Name the blood parasite species.
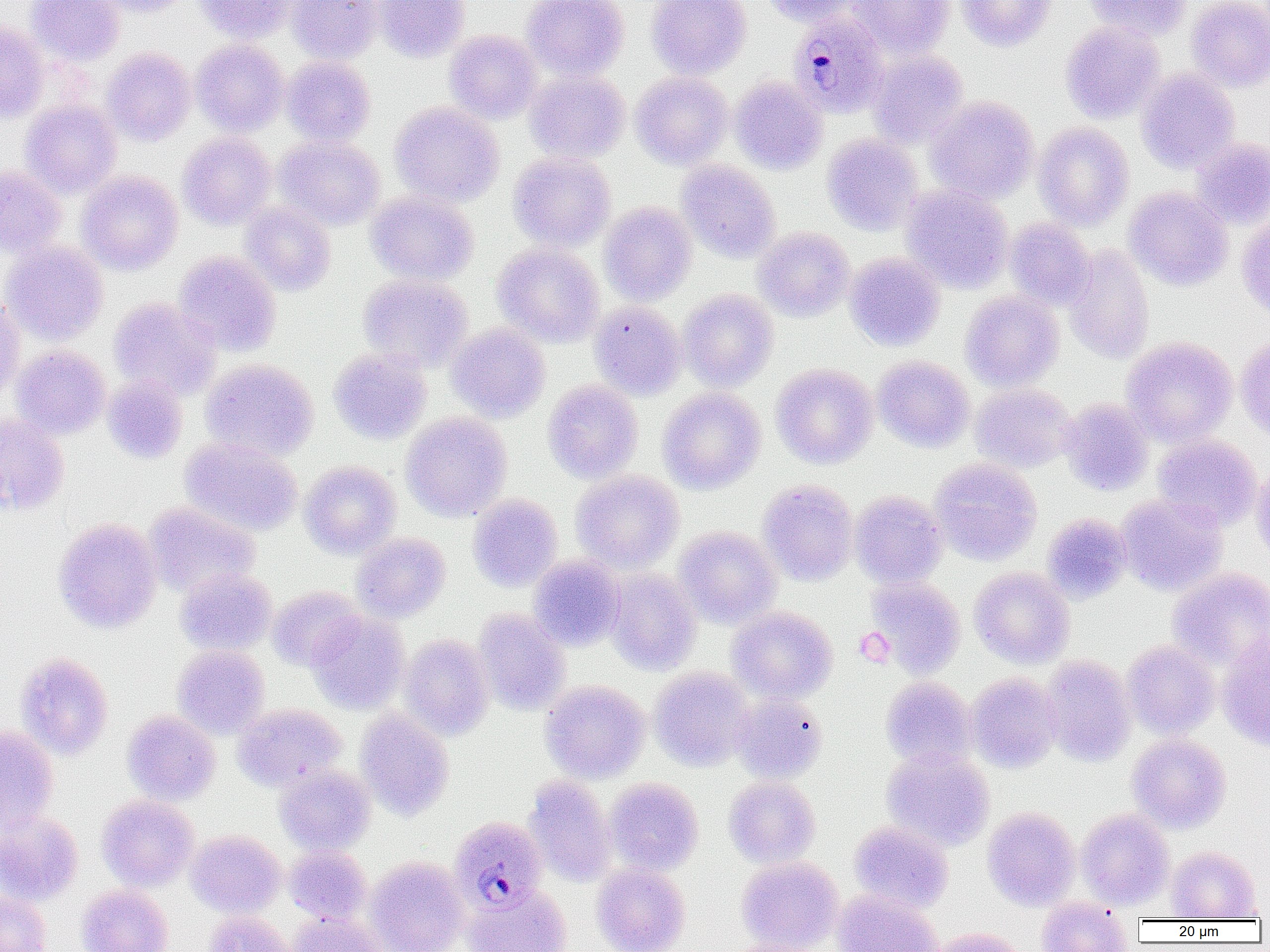

Plasmodium malariae.

Summary:
  - Coordinate format: approximate bounding boxes as named x1/y1/x2/y2 corners in pixels
  - Uninfected red blood cell locations: (x1=26, y1=0, x2=125, y2=65), (x1=91, y1=0, x2=196, y2=18), (x1=194, y1=0, x2=296, y2=43), (x1=286, y1=0, x2=383, y2=63), (x1=373, y1=0, x2=470, y2=62), (x1=521, y1=0, x2=629, y2=81), (x1=647, y1=0, x2=751, y2=79), (x1=761, y1=0, x2=857, y2=26), (x1=847, y1=0, x2=954, y2=59), (x1=957, y1=0, x2=1057, y2=51), (x1=1085, y1=0, x2=1192, y2=40), (x1=1186, y1=0, x2=1270, y2=92), (x1=1059, y1=21, x2=1165, y2=123), (x1=0, y1=22, x2=50, y2=122), (x1=445, y1=30, x2=543, y2=124), (x1=191, y1=40, x2=289, y2=136), (x1=101, y1=47, x2=196, y2=145), (x1=868, y1=50, x2=968, y2=148), (x1=281, y1=56, x2=375, y2=146), (x1=524, y1=69, x2=630, y2=163), (x1=1137, y1=69, x2=1240, y2=173), (x1=630, y1=72, x2=733, y2=169), (x1=730, y1=75, x2=827, y2=175), (x1=925, y1=96, x2=1039, y2=204), (x1=21, y1=101, x2=122, y2=198), (x1=390, y1=101, x2=503, y2=207), (x1=1034, y1=122, x2=1134, y2=231), (x1=178, y1=132, x2=277, y2=229), (x1=822, y1=133, x2=923, y2=235), (x1=275, y1=136, x2=386, y2=230), (x1=1191, y1=136, x2=1270, y2=229), (x1=508, y1=152, x2=616, y2=251), (x1=676, y1=160, x2=781, y2=262), (x1=0, y1=165, x2=65, y2=257), (x1=77, y1=171, x2=183, y2=275), (x1=900, y1=184, x2=1014, y2=292), (x1=1124, y1=187, x2=1234, y2=291), (x1=365, y1=190, x2=479, y2=286), (x1=239, y1=202, x2=336, y2=296), (x1=598, y1=202, x2=697, y2=305), (x1=1236, y1=213, x2=1270, y2=321), (x1=1004, y1=218, x2=1094, y2=309), (x1=753, y1=227, x2=855, y2=321), (x1=1, y1=241, x2=108, y2=345), (x1=493, y1=243, x2=604, y2=346), (x1=1063, y1=245, x2=1154, y2=363), (x1=173, y1=251, x2=281, y2=357), (x1=844, y1=251, x2=945, y2=351), (x1=357, y1=274, x2=473, y2=371), (x1=678, y1=289, x2=779, y2=391), (x1=960, y1=290, x2=1064, y2=391), (x1=0, y1=294, x2=25, y2=401), (x1=109, y1=297, x2=220, y2=401), (x1=589, y1=301, x2=687, y2=400), (x1=446, y1=323, x2=550, y2=422), (x1=1235, y1=334, x2=1270, y2=439), (x1=1121, y1=337, x2=1237, y2=448), (x1=11, y1=346, x2=110, y2=439), (x1=328, y1=348, x2=432, y2=445), (x1=872, y1=356, x2=975, y2=452), (x1=201, y1=358, x2=319, y2=460), (x1=771, y1=363, x2=878, y2=468), (x1=101, y1=373, x2=188, y2=464), (x1=543, y1=379, x2=643, y2=483), (x1=970, y1=383, x2=1077, y2=474), (x1=657, y1=387, x2=766, y2=494), (x1=1059, y1=398, x2=1154, y2=495), (x1=401, y1=412, x2=512, y2=521), (x1=0, y1=413, x2=69, y2=514), (x1=1153, y1=436, x2=1262, y2=530), (x1=180, y1=438, x2=303, y2=536), (x1=929, y1=458, x2=1042, y2=565), (x1=300, y1=461, x2=401, y2=558), (x1=1251, y1=461, x2=1270, y2=563), (x1=570, y1=470, x2=684, y2=573), (x1=758, y1=480, x2=858, y2=585), (x1=850, y1=490, x2=948, y2=588), (x1=1116, y1=493, x2=1228, y2=596), (x1=467, y1=494, x2=563, y2=592), (x1=143, y1=502, x2=261, y2=597), (x1=1041, y1=512, x2=1131, y2=604), (x1=52, y1=517, x2=162, y2=633), (x1=673, y1=526, x2=782, y2=628), (x1=352, y1=532, x2=451, y2=622), (x1=529, y1=555, x2=626, y2=651), (x1=176, y1=567, x2=277, y2=655), (x1=969, y1=567, x2=1075, y2=668), (x1=1166, y1=567, x2=1270, y2=671), (x1=606, y1=569, x2=701, y2=675), (x1=866, y1=577, x2=966, y2=677), (x1=266, y1=585, x2=363, y2=670), (x1=727, y1=606, x2=838, y2=704), (x1=473, y1=608, x2=570, y2=715), (x1=307, y1=612, x2=409, y2=714), (x1=1216, y1=631, x2=1270, y2=751), (x1=399, y1=634, x2=495, y2=740), (x1=1121, y1=641, x2=1220, y2=739), (x1=172, y1=645, x2=269, y2=738), (x1=15, y1=652, x2=114, y2=759), (x1=1040, y1=654, x2=1137, y2=767), (x1=648, y1=667, x2=755, y2=771), (x1=966, y1=673, x2=1062, y2=772), (x1=880, y1=677, x2=976, y2=769), (x1=540, y1=680, x2=650, y2=783), (x1=731, y1=695, x2=827, y2=784), (x1=232, y1=703, x2=347, y2=791), (x1=355, y1=709, x2=454, y2=821), (x1=122, y1=710, x2=220, y2=805), (x1=0, y1=725, x2=58, y2=833), (x1=1127, y1=733, x2=1231, y2=833), (x1=882, y1=747, x2=995, y2=851), (x1=274, y1=765, x2=375, y2=855), (x1=524, y1=775, x2=617, y2=887), (x1=723, y1=776, x2=821, y2=868), (x1=605, y1=777, x2=703, y2=875), (x1=96, y1=795, x2=199, y2=891), (x1=982, y1=807, x2=1081, y2=910), (x1=1076, y1=808, x2=1175, y2=910), (x1=0, y1=812, x2=83, y2=906), (x1=849, y1=820, x2=953, y2=913), (x1=186, y1=830, x2=285, y2=918), (x1=284, y1=845, x2=372, y2=924), (x1=1166, y1=846, x2=1261, y2=920), (x1=736, y1=856, x2=843, y2=952), (x1=367, y1=857, x2=470, y2=952), (x1=591, y1=862, x2=691, y2=952), (x1=76, y1=884, x2=173, y2=952), (x1=464, y1=884, x2=572, y2=952), (x1=832, y1=889, x2=944, y2=952), (x1=0, y1=891, x2=52, y2=951), (x1=1035, y1=898, x2=1134, y2=951), (x1=204, y1=910, x2=296, y2=952), (x1=288, y1=912, x2=389, y2=952), (x1=927, y1=927, x2=1030, y2=952), (x1=726, y1=938, x2=829, y2=952)
  - Plasmodium malariae-infected red blood cell locations: (x1=788, y1=11, x2=889, y2=118), (x1=449, y1=815, x2=547, y2=912)
  - Platelet locations: (x1=854, y1=628, x2=894, y2=666)
  - Magnification: 1000x
  - Preparation: thin blood film
  - Modality: light microscopy
  - Image size: 1270×952 pixels
  - Field of view: single